Report the malaria status of this cell.
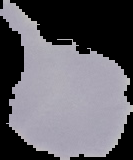

It is uninfected.

From a thin blood smear. Image is 133×160 pixels. The area outside the segmented cell region is set to black.